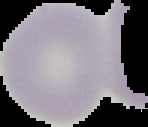
Summary:
  - Image size: 148×127 pixels
  - Image type: cell region segmented out of the field of view; surrounding area masked to black
  - Preparation: thin blood film
  - Malaria status: uninfected